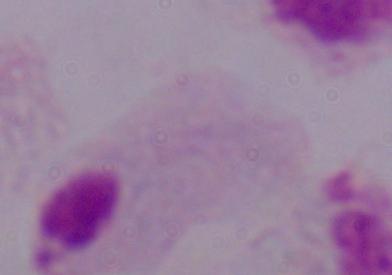

Photomicrograph. A trichomonad is seen. 1000x magnification.